State the preparation type.
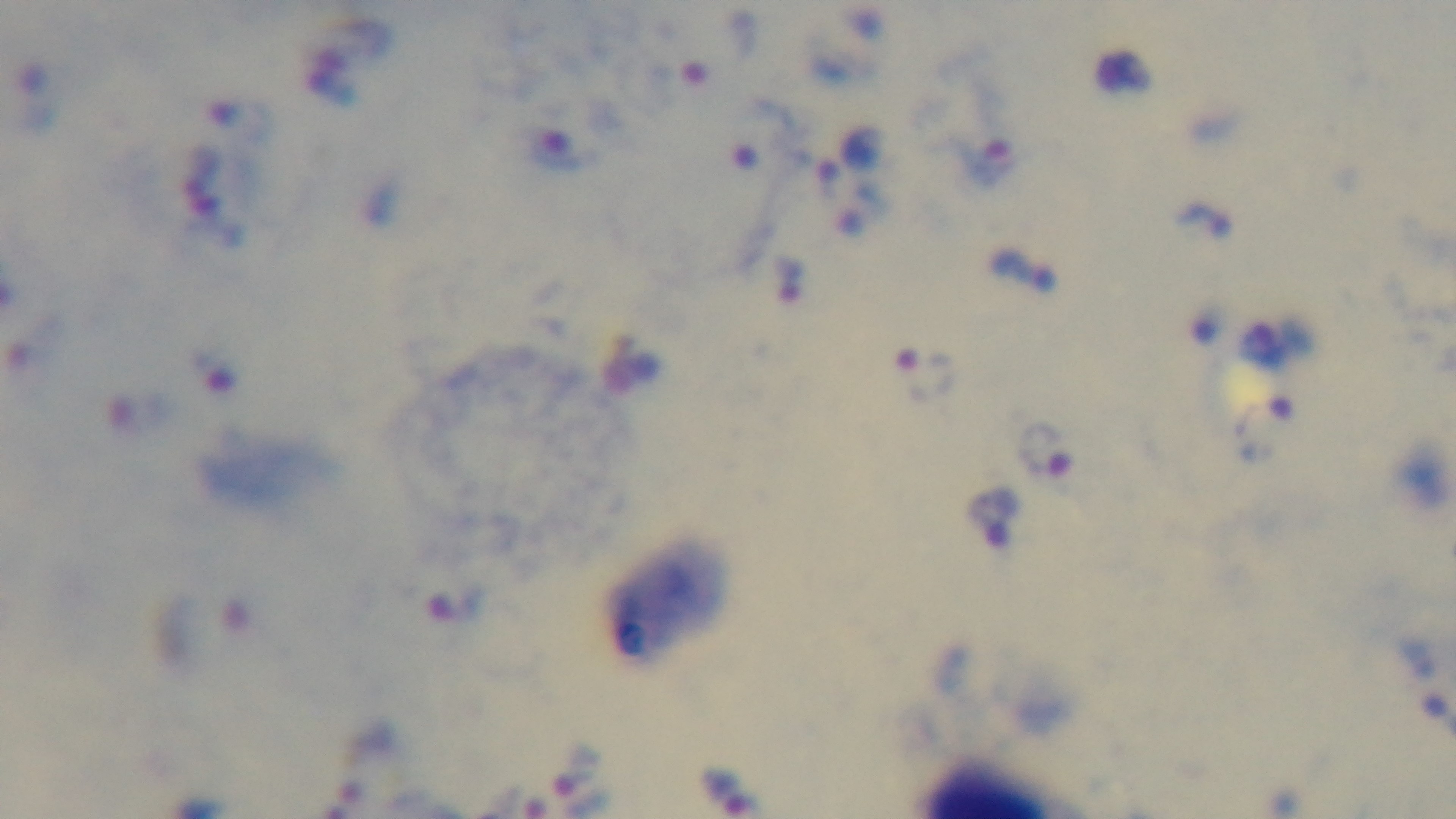
Thick.

Summary:
  - Field of view: single
  - Malaria status: positive
  - Modality: light microscopy
  - Stain: Giemsa
  - Capture: mounted 4K digital camera
  - Objective: 100x oil immersion